Locate every Plasmodium parasite.
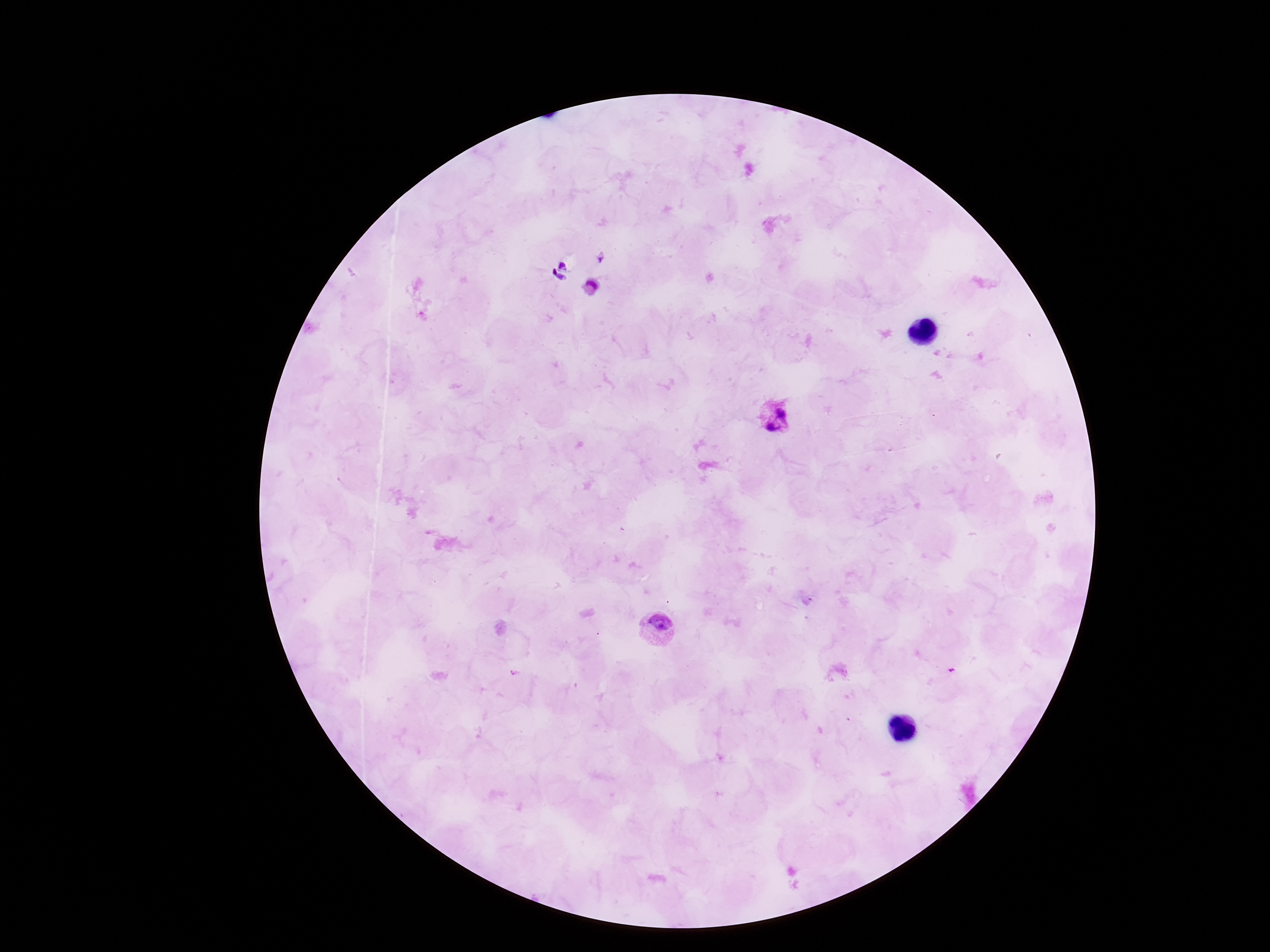
Approximate object centers, in pixels from the top-left corner.
Plasmodium parasites: (x=773, y=416), (x=660, y=630).

100x magnification. Smartphone photograph taken through the microscope eyepiece. Image is 1270×952 pixels. Thick peripheral-blood smear. Single field of view. Patient malaria status: positive. Giemsa stain.